Report the malaria status of this cell.
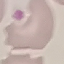

It is uninfected.

stain: Giemsa
image_type: cell patch, automatically extracted from a larger field of view and resized to 64 × 64 pixels
preparation: thin smear
capture: smartphone camera at the microscope eyepiece